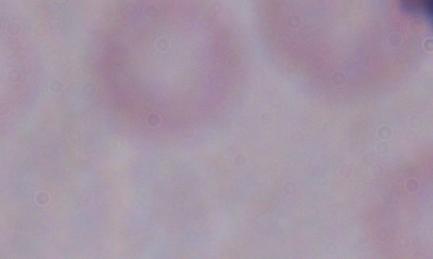

Summary:
  - Magnification: 1000x
  - Identification: trypanosome
  - Modality: photomicrograph